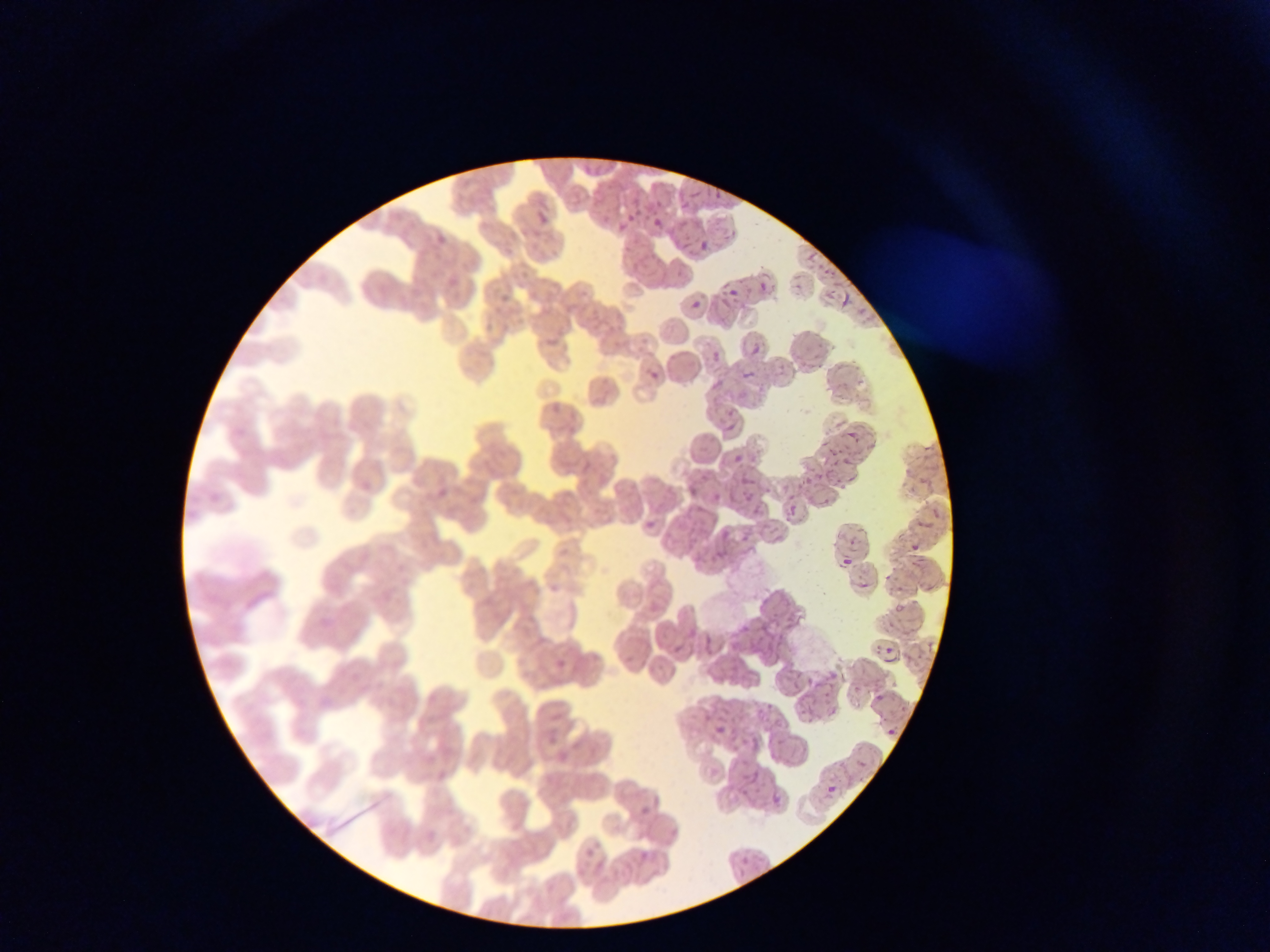
Approximate bounding boxes as [left, top, right, bottom] in pixels.
Summary:
  - Plasmodium parasite locations: [710, 188, 719, 198], [689, 192, 700, 202], [537, 211, 551, 223], [624, 215, 632, 222], [653, 218, 663, 227], [620, 225, 628, 230], [699, 241, 710, 252], [806, 252, 817, 264], [760, 283, 769, 293], [728, 288, 739, 298], [840, 291, 851, 310], [691, 302, 700, 310], [753, 346, 762, 355], [712, 352, 721, 361], [744, 370, 754, 378], [649, 371, 659, 380], [726, 425, 735, 434], [849, 430, 861, 444], [828, 449, 839, 458], [734, 455, 744, 464], [843, 458, 853, 472], [826, 466, 831, 483], [742, 476, 752, 485], [847, 478, 858, 484], [689, 487, 698, 496], [817, 500, 830, 506], [787, 509, 797, 520], [646, 520, 656, 529], [723, 530, 732, 539], [905, 541, 922, 551], [843, 557, 852, 567], [859, 581, 869, 590], [896, 606, 906, 616], [702, 633, 716, 647], [666, 640, 680, 652], [702, 651, 712, 660], [881, 657, 900, 665], [556, 658, 566, 668], [824, 674, 836, 683], [807, 676, 816, 686], [875, 693, 885, 703], [828, 706, 838, 717], [774, 718, 786, 730], [871, 721, 895, 736], [715, 725, 726, 736], [745, 769, 762, 785], [824, 785, 838, 797], [771, 793, 785, 805]
  - Country: Ghana
  - Field of view: single
  - Image size: 1270×952 pixels
  - Preparation: thin blood film
  - Capture: mobile-phone photograph through a microscope